Comment on the morphology of the erythrocytes.
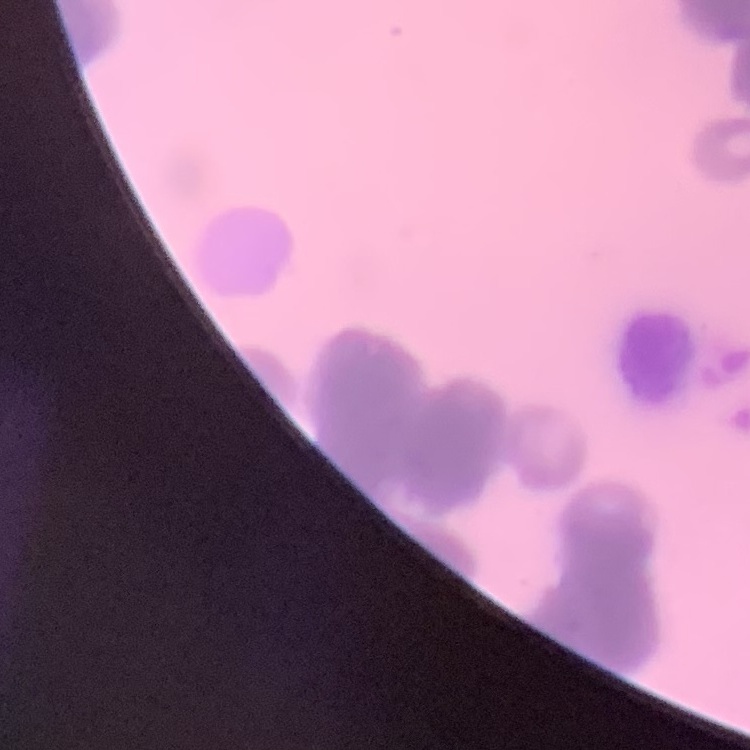

Rouleaux formation.

Thin blood film. Field's or Giemsa stain. One tile cut from a larger photomicrograph.